Name the cell type shown.
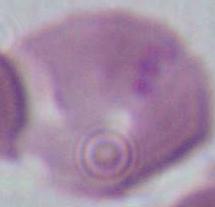

An erythrocyte.

magnification = 1000x
modality = photomicrograph